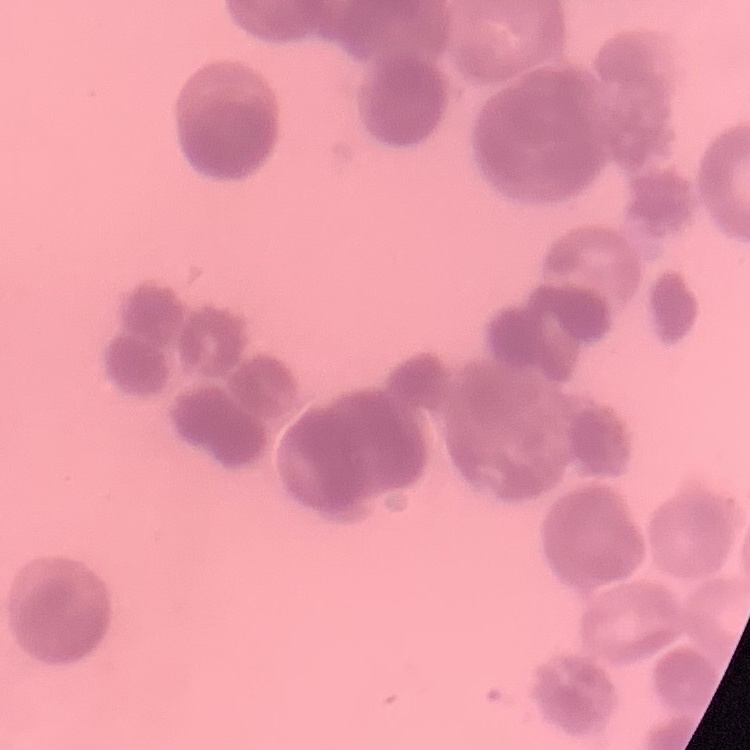 The red blood cells show rouleaux formation. Square crop of a larger photomicrograph. Thin blood smear. Stained with either Field's or Giemsa.